Give the position of every leukocyte visible.
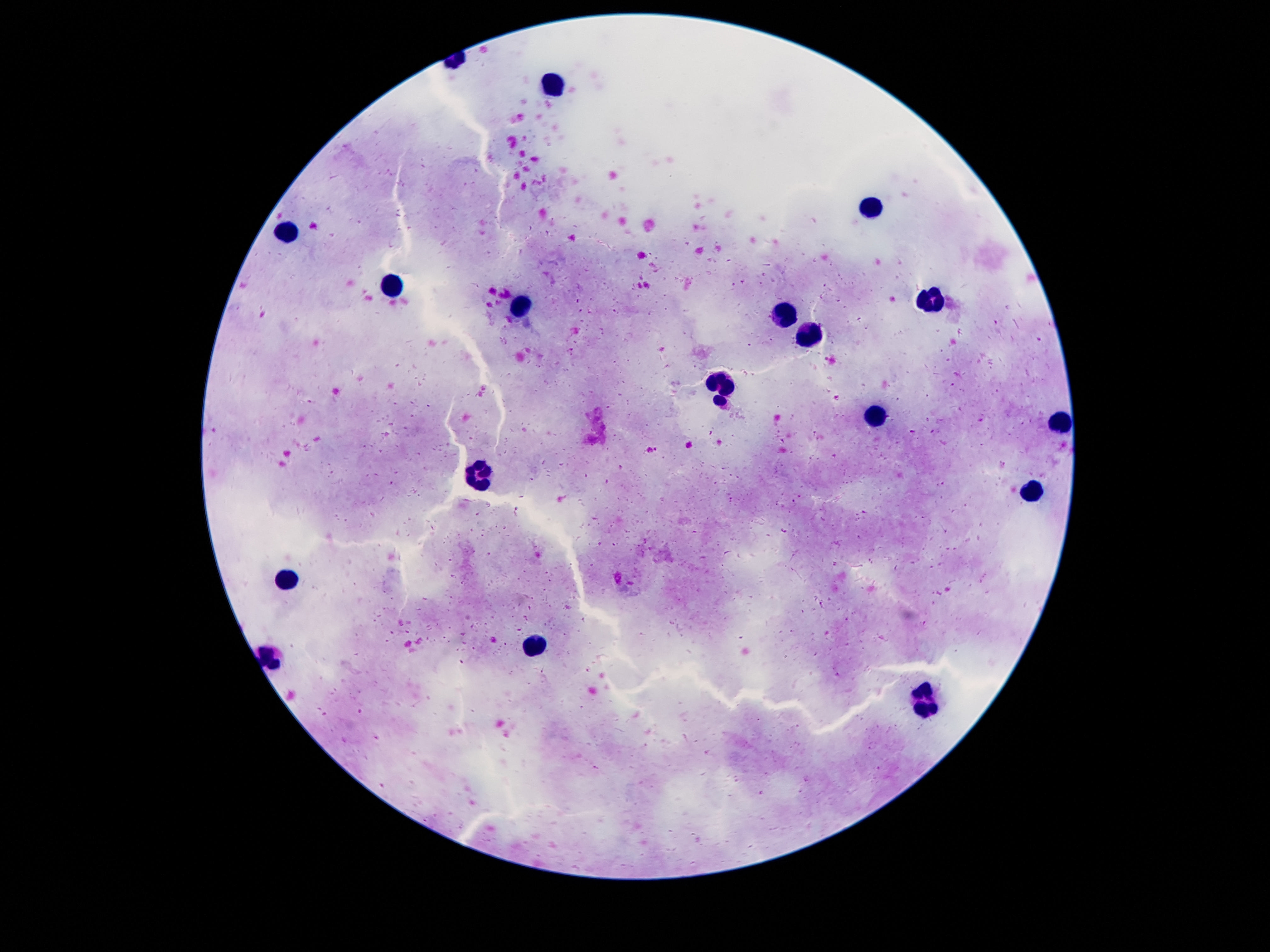

Approximate object centers, in pixels from the top-left corner.
Leukocytes: (x=548, y=85), (x=870, y=207), (x=286, y=233), (x=394, y=287), (x=930, y=299), (x=522, y=306), (x=786, y=313), (x=807, y=334), (x=720, y=389), (x=876, y=415), (x=1061, y=422), (x=478, y=476), (x=1033, y=493), (x=288, y=580), (x=536, y=644), (x=925, y=704).

Single field of view. 100x magnification. Giemsa stain. Image is 1270×952 pixels. Patient malaria status: negative. Thick peripheral-blood smear. Smartphone photograph taken through the microscope eyepiece.